Outline each blood parasite and name the species.
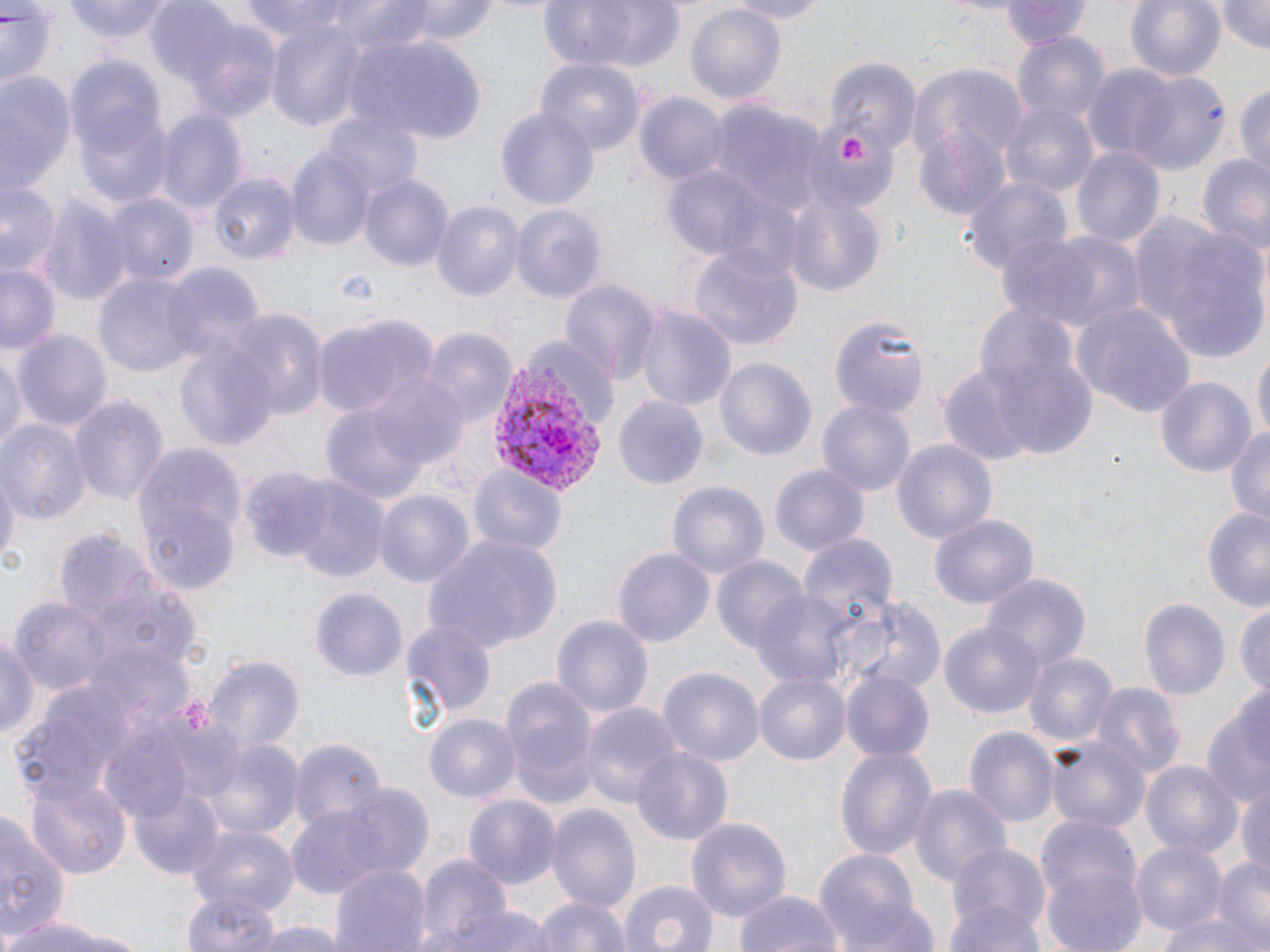

Approximate bounding boxes as named x1/y1/x2/y2 corners in pixels.
Plasmodium vivax-infected red blood cells: (x1=493, y1=344, x2=616, y2=494).
No Plasmodium falciparum, Plasmodium ovale, Plasmodium malariae, Babesia divergens, or Trypanosoma brucei observed.

Uninfected red blood cell locations: (x1=64, y1=0, x2=176, y2=45), (x1=238, y1=0, x2=391, y2=44), (x1=388, y1=0, x2=503, y2=44), (x1=536, y1=0, x2=685, y2=72), (x1=717, y1=0, x2=834, y2=22), (x1=996, y1=0, x2=1093, y2=47), (x1=1123, y1=0, x2=1227, y2=83), (x1=1215, y1=0, x2=1268, y2=56), (x1=0, y1=3, x2=60, y2=94), (x1=155, y1=6, x2=280, y2=124), (x1=687, y1=6, x2=784, y2=105), (x1=263, y1=24, x2=367, y2=126), (x1=1010, y1=31, x2=1110, y2=137), (x1=346, y1=32, x2=488, y2=140), (x1=823, y1=55, x2=918, y2=153), (x1=537, y1=59, x2=644, y2=155), (x1=68, y1=61, x2=170, y2=208), (x1=1083, y1=64, x2=1187, y2=164), (x1=912, y1=65, x2=1028, y2=167), (x1=0, y1=70, x2=75, y2=199), (x1=1129, y1=71, x2=1231, y2=178), (x1=1236, y1=77, x2=1270, y2=180), (x1=633, y1=93, x2=726, y2=188), (x1=998, y1=100, x2=1099, y2=200), (x1=706, y1=102, x2=830, y2=217), (x1=495, y1=108, x2=599, y2=210), (x1=156, y1=109, x2=245, y2=217), (x1=325, y1=109, x2=424, y2=201), (x1=809, y1=119, x2=896, y2=210), (x1=915, y1=127, x2=1010, y2=220), (x1=287, y1=147, x2=377, y2=253), (x1=1071, y1=147, x2=1166, y2=252), (x1=1198, y1=152, x2=1270, y2=256), (x1=660, y1=167, x2=778, y2=265), (x1=358, y1=171, x2=454, y2=275), (x1=207, y1=173, x2=298, y2=266), (x1=960, y1=174, x2=1070, y2=278), (x1=1, y1=180, x2=63, y2=278), (x1=782, y1=189, x2=887, y2=301), (x1=104, y1=194, x2=196, y2=289), (x1=40, y1=195, x2=134, y2=307), (x1=433, y1=200, x2=525, y2=304), (x1=511, y1=204, x2=607, y2=303), (x1=1004, y1=227, x2=1143, y2=334), (x1=1154, y1=227, x2=1268, y2=363), (x1=687, y1=246, x2=800, y2=353), (x1=0, y1=260, x2=64, y2=357), (x1=162, y1=266, x2=264, y2=365), (x1=93, y1=271, x2=205, y2=381), (x1=561, y1=280, x2=657, y2=383), (x1=967, y1=299, x2=1092, y2=434), (x1=1075, y1=302, x2=1197, y2=421), (x1=636, y1=306, x2=736, y2=415), (x1=222, y1=308, x2=325, y2=425), (x1=313, y1=315, x2=435, y2=418), (x1=833, y1=316, x2=930, y2=422), (x1=15, y1=328, x2=110, y2=433), (x1=421, y1=329, x2=515, y2=429), (x1=172, y1=337, x2=279, y2=451), (x1=1252, y1=346, x2=1269, y2=447), (x1=984, y1=347, x2=1103, y2=461), (x1=0, y1=349, x2=23, y2=458), (x1=716, y1=356, x2=815, y2=465), (x1=939, y1=368, x2=1038, y2=468), (x1=1153, y1=373, x2=1260, y2=477), (x1=365, y1=374, x2=471, y2=472), (x1=70, y1=394, x2=169, y2=510), (x1=612, y1=395, x2=708, y2=491), (x1=817, y1=399, x2=915, y2=500), (x1=324, y1=402, x2=433, y2=507), (x1=0, y1=419, x2=89, y2=527), (x1=1224, y1=423, x2=1270, y2=525), (x1=892, y1=438, x2=997, y2=547), (x1=136, y1=452, x2=242, y2=593), (x1=770, y1=463, x2=869, y2=558), (x1=0, y1=464, x2=18, y2=573), (x1=468, y1=468, x2=566, y2=561), (x1=283, y1=480, x2=387, y2=580), (x1=669, y1=480, x2=769, y2=583), (x1=374, y1=489, x2=474, y2=587), (x1=1201, y1=507, x2=1270, y2=611), (x1=928, y1=511, x2=1040, y2=612), (x1=421, y1=534, x2=562, y2=652), (x1=799, y1=534, x2=899, y2=639), (x1=612, y1=547, x2=716, y2=650), (x1=709, y1=553, x2=810, y2=659), (x1=984, y1=574, x2=1089, y2=674), (x1=310, y1=588, x2=408, y2=681), (x1=748, y1=591, x2=859, y2=693), (x1=1233, y1=594, x2=1270, y2=700), (x1=11, y1=595, x2=117, y2=697), (x1=846, y1=596, x2=945, y2=699), (x1=1138, y1=598, x2=1231, y2=701), (x1=548, y1=611, x2=655, y2=723), (x1=402, y1=620, x2=495, y2=721), (x1=939, y1=622, x2=1044, y2=719), (x1=0, y1=631, x2=41, y2=747), (x1=83, y1=645, x2=196, y2=739), (x1=1023, y1=648, x2=1118, y2=748), (x1=203, y1=655, x2=307, y2=758), (x1=657, y1=666, x2=762, y2=766), (x1=840, y1=670, x2=936, y2=763), (x1=754, y1=672, x2=849, y2=766), (x1=499, y1=674, x2=597, y2=806), (x1=1090, y1=682, x2=1185, y2=782), (x1=13, y1=686, x2=132, y2=797), (x1=1199, y1=695, x2=1270, y2=810), (x1=579, y1=702, x2=682, y2=810), (x1=100, y1=707, x2=233, y2=820), (x1=423, y1=713, x2=521, y2=803), (x1=963, y1=726, x2=1058, y2=830), (x1=286, y1=738, x2=388, y2=830), (x1=1048, y1=739, x2=1149, y2=829), (x1=212, y1=740, x2=302, y2=840), (x1=834, y1=745, x2=936, y2=865), (x1=631, y1=747, x2=733, y2=845), (x1=1141, y1=761, x2=1240, y2=859), (x1=26, y1=776, x2=133, y2=876), (x1=1234, y1=778, x2=1270, y2=882), (x1=291, y1=783, x2=432, y2=896), (x1=909, y1=784, x2=1012, y2=896), (x1=132, y1=787, x2=225, y2=879), (x1=463, y1=795, x2=559, y2=889), (x1=546, y1=802, x2=640, y2=915), (x1=0, y1=810, x2=67, y2=941), (x1=685, y1=815, x2=791, y2=925), (x1=188, y1=824, x2=297, y2=916), (x1=1132, y1=837, x2=1228, y2=939), (x1=946, y1=840, x2=1049, y2=941), (x1=1036, y1=843, x2=1148, y2=952), (x1=812, y1=849, x2=924, y2=952), (x1=419, y1=855, x2=512, y2=948), (x1=1214, y1=856, x2=1270, y2=945), (x1=328, y1=860, x2=432, y2=952), (x1=617, y1=878, x2=720, y2=952), (x1=731, y1=888, x2=844, y2=952), (x1=183, y1=892, x2=282, y2=951), (x1=533, y1=895, x2=632, y2=952), (x1=944, y1=902, x2=1047, y2=952), (x1=442, y1=903, x2=550, y2=952), (x1=838, y1=903, x2=943, y2=952), (x1=1161, y1=912, x2=1258, y2=952), (x1=2, y1=913, x2=111, y2=952), (x1=251, y1=919, x2=347, y2=952). Platelet locations: (x1=836, y1=133, x2=868, y2=165). Slide-level diagnosis: Plasmodium vivax. Single field of view. Thin blood smear. Optical microscopy. May-Grünwald-Giemsa-stained preparation. Image is 1270×952 pixels. 1000x magnification.